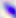
Toxoplasma gondii is shown. Photomicrograph. 400x magnification.